Classify this cell by malaria status.
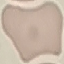

It is uninfected.

Giemsa stain. Automatically extracted cell patch, resized to 64 × 64 pixels. Thin blood smear. Photographed with a smartphone camera at the microscope eyepiece.